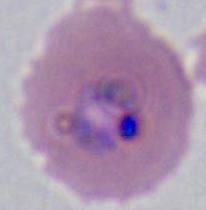
modality = photomicrograph
magnification = 400x or 1000x
identification = Plasmodium